Locate every uninfected red blood cell.
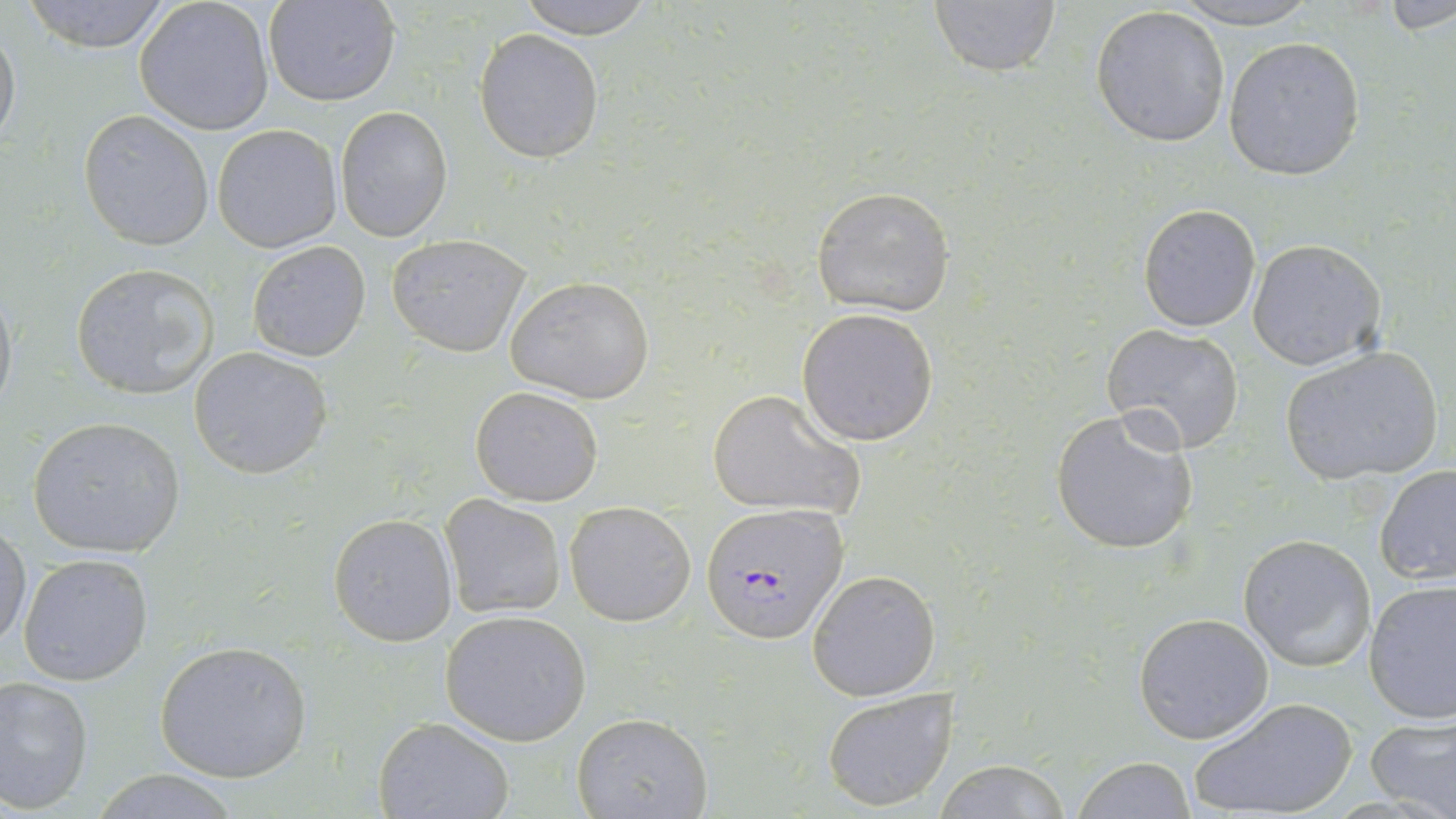

Approximate bounding boxes as [x1, y1, x2, y2] in pixels.
Uninfected red blood cells: [19, 0, 179, 53], [133, 0, 276, 135], [264, 0, 402, 106], [512, 0, 664, 37], [1161, 0, 1321, 27], [925, 1, 1063, 79], [1381, 1, 1456, 36], [1090, 5, 1232, 148], [0, 23, 21, 150], [474, 29, 604, 163], [1223, 35, 1366, 182], [335, 106, 452, 242], [79, 110, 215, 251], [212, 125, 342, 253], [811, 186, 956, 315], [1139, 203, 1262, 331], [385, 235, 530, 355], [1247, 239, 1387, 370], [246, 240, 371, 361], [71, 262, 223, 400], [503, 275, 656, 404], [0, 280, 18, 423], [796, 307, 939, 446], [1101, 324, 1246, 452], [1278, 346, 1446, 488], [189, 347, 333, 479], [470, 385, 605, 504], [706, 388, 864, 521], [1050, 407, 1202, 556], [26, 417, 187, 558], [1375, 466, 1456, 587], [441, 495, 566, 619], [564, 501, 696, 627], [328, 512, 457, 646], [0, 521, 31, 650], [1237, 534, 1377, 672], [17, 552, 153, 687], [808, 570, 941, 702], [1363, 580, 1456, 724], [439, 609, 592, 745], [1133, 612, 1274, 744], [154, 640, 313, 783], [0, 673, 95, 813], [822, 687, 959, 812], [1189, 696, 1359, 818], [572, 713, 713, 819], [1365, 715, 1456, 818], [372, 716, 515, 819], [1075, 757, 1198, 817], [930, 759, 1074, 818], [92, 771, 245, 818].

{
  "slide_level_diagnosis": "Plasmodium falciparum",
  "image_size": "1456×819 pixels",
  "stain": "May-Grünwald-Giemsa",
  "modality": "light microscopy",
  "plasmodium_falciparum_infected_red_blood_cell_locations": "approximate bounding boxes as [x1, y1, x2, y2] in pixels: [702, 504, 851, 643]",
  "magnification": "1000x",
  "preparation": "thin blood smear",
  "field_of_view": "one of a larger specimen"
}